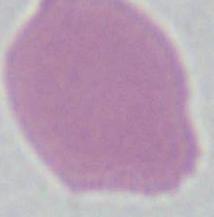
identification = red blood cell
modality = micrograph
magnification = 1000x